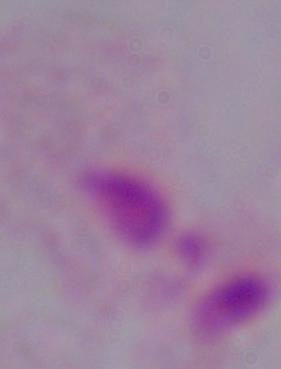

magnification: 1000x
identification: trichomonad
modality: micrograph